Give the preparation type.
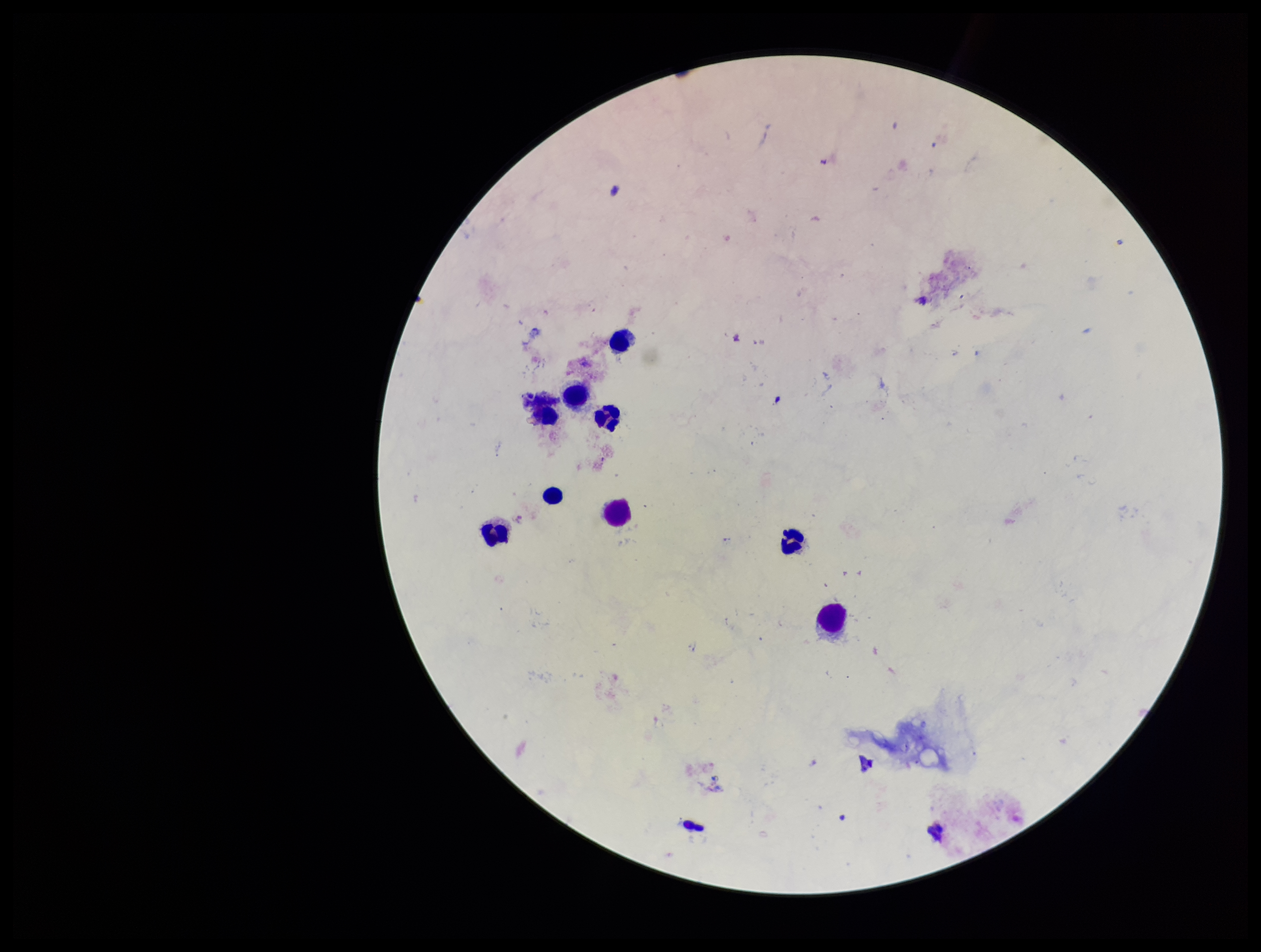
A thick smear.

Summary:
  - Plasmodium parasites: none identified
  - Patient malaria status: negative
  - Stain: Giemsa
  - Field of view: single
  - Leukocyte count: 9
  - Parasite count: 0
  - Capture: smartphone photograph through the microscope eyepiece
  - Image size: 1261×952 pixels